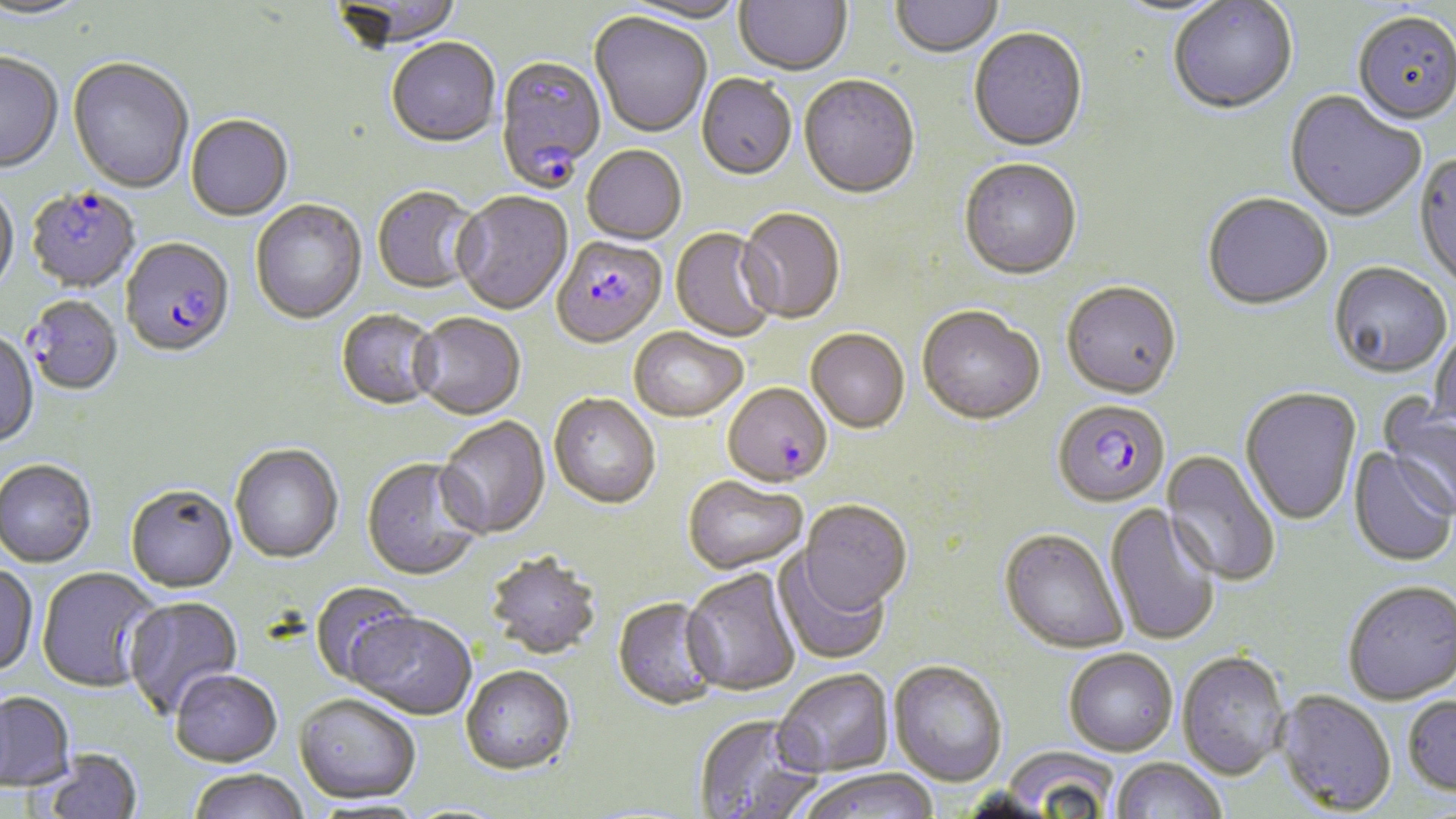

Summary:
  - Coordinate format: approximate bounding boxes as [x1, y1, x2, y2] in pixels
  - Plasmodium falciparum-infected red blood cell locations: [494, 57, 606, 193], [26, 187, 140, 293], [551, 238, 666, 351], [120, 239, 235, 360], [23, 296, 122, 397], [723, 384, 832, 490], [1058, 403, 1175, 511]
  - Uninfected red blood cell locations: [0, 0, 93, 21], [331, 0, 464, 51], [618, 0, 748, 26], [733, 0, 853, 78], [890, 1, 1004, 59], [1107, 1, 1235, 21], [1168, 1, 1298, 117], [1352, 13, 1456, 128], [589, 14, 712, 140], [968, 29, 1088, 155], [386, 40, 501, 149], [0, 54, 63, 175], [67, 59, 193, 194], [697, 76, 797, 183], [798, 77, 920, 201], [1284, 91, 1425, 224], [186, 117, 293, 221], [582, 148, 686, 246], [1413, 153, 1456, 293], [959, 161, 1082, 282], [0, 183, 19, 298], [372, 188, 483, 295], [452, 193, 573, 316], [1202, 195, 1333, 312], [250, 201, 367, 325], [737, 209, 845, 326], [670, 230, 778, 344], [1328, 264, 1452, 381], [1061, 284, 1182, 403], [917, 308, 1045, 428], [336, 310, 443, 410], [411, 314, 526, 421], [1429, 322, 1456, 436], [628, 329, 747, 424], [0, 330, 39, 448], [805, 330, 910, 435], [1240, 388, 1362, 526], [1379, 394, 1456, 522], [549, 395, 660, 510], [436, 417, 550, 541], [229, 443, 344, 564], [1349, 448, 1455, 567], [1161, 450, 1281, 587], [362, 458, 485, 582], [0, 459, 97, 568], [683, 477, 808, 576], [125, 484, 237, 592], [798, 501, 912, 616], [1105, 503, 1221, 647], [999, 529, 1128, 655], [772, 550, 891, 666], [485, 552, 602, 661], [0, 563, 38, 676], [37, 567, 162, 692], [682, 569, 800, 697], [1342, 580, 1456, 704], [309, 581, 422, 687], [123, 596, 244, 718], [612, 598, 723, 712], [350, 613, 477, 721], [1064, 649, 1178, 756], [1176, 650, 1290, 779], [888, 661, 1007, 787], [460, 667, 575, 777], [169, 670, 282, 767], [773, 671, 894, 778], [1275, 689, 1396, 815], [0, 692, 76, 792], [294, 694, 421, 805], [1403, 694, 1456, 795], [693, 714, 822, 819], [1002, 746, 1120, 816], [40, 749, 143, 818], [1109, 757, 1227, 818], [188, 769, 310, 819], [797, 769, 940, 819]
  - Slide-level diagnosis: Plasmodium falciparum
  - Magnification: 1000x
  - Stain: May-Grünwald-Giemsa
  - Preparation: thin blood smear
  - Field of view: single
  - Image size: 1456×819 pixels
  - Modality: optical microscopy